Locate every blood parasite and identify its species.
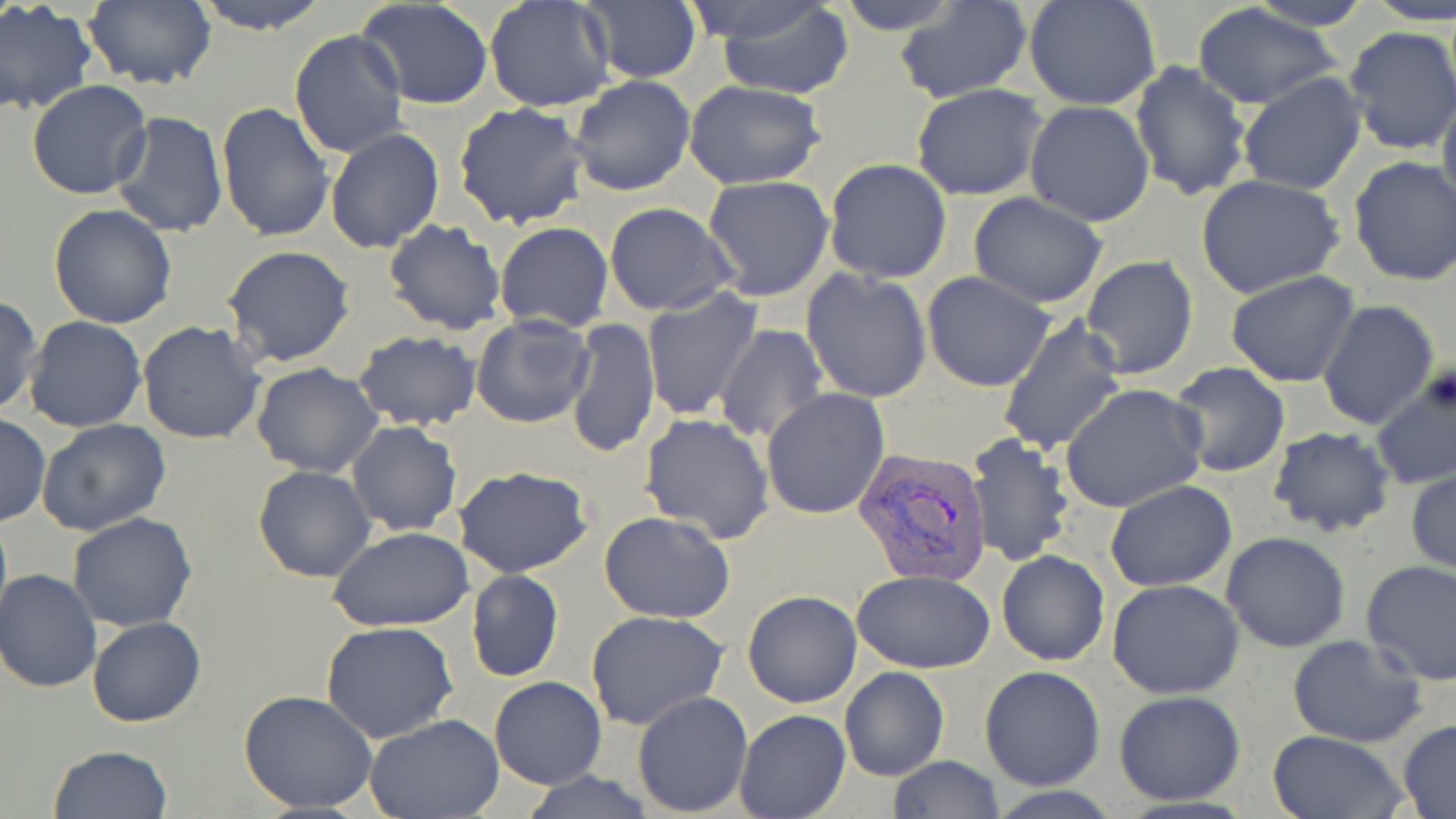

Approximate bounding boxes as [x1, y1, x2, y2] in pixels.
Plasmodium vivax-infected red blood cells: [852, 447, 991, 588].
No Plasmodium falciparum, Plasmodium ovale, Plasmodium malariae, Babesia divergens, or Trypanosoma brucei observed.

slide_level_diagnosis: Plasmodium vivax
preparation: thin blood film
modality: optical microscopy
image_size: 1456×819 pixels
stain: May-Grünwald-Giemsa
uninfected_red_blood_cell_locations: 'approximate bounding boxes as [x1, y1, x2, y2] in pixels: [80, 0, 217, 90], [183, 0, 334, 35], [714, 0, 855, 99], [838, 0, 960, 31], [1023, 0, 1164, 111], [1242, 0, 1373, 30], [1366, 0, 1454, 26], [485, 1, 618, 112], [895, 1, 1034, 104], [356, 2, 494, 109], [576, 2, 704, 84], [0, 3, 97, 116], [1191, 5, 1343, 109], [1341, 26, 1455, 157], [289, 29, 410, 160], [1128, 61, 1253, 201], [1238, 72, 1368, 193], [569, 74, 696, 196], [27, 80, 154, 200], [682, 80, 826, 188], [1437, 84, 1456, 218], [911, 85, 1047, 202], [216, 101, 336, 244], [453, 101, 590, 231], [1024, 101, 1156, 227], [111, 110, 230, 238], [324, 127, 444, 254], [1347, 156, 1456, 287], [823, 158, 952, 283], [1196, 174, 1346, 300], [702, 175, 834, 301], [968, 193, 1109, 309], [618, 197, 747, 418], [603, 203, 737, 316], [46, 204, 177, 330], [383, 219, 507, 335], [494, 221, 614, 332], [222, 246, 356, 368], [1079, 254, 1200, 379], [801, 268, 934, 403], [922, 270, 1056, 392], [1227, 271, 1360, 387], [641, 288, 762, 421], [0, 296, 43, 416], [1317, 300, 1439, 432], [471, 313, 595, 429], [23, 316, 147, 434], [997, 316, 1127, 457], [565, 318, 661, 459], [138, 319, 267, 445], [715, 324, 829, 446], [354, 330, 481, 433], [1169, 362, 1290, 478], [251, 363, 383, 478], [1371, 368, 1455, 490], [1060, 384, 1207, 514], [762, 388, 893, 520], [639, 413, 775, 542], [0, 414, 49, 526], [36, 420, 170, 537], [347, 421, 462, 535], [1267, 426, 1396, 538], [964, 433, 1077, 568], [252, 465, 375, 584], [455, 465, 593, 577], [1407, 470, 1455, 576], [1105, 481, 1238, 590], [0, 507, 12, 633], [68, 512, 198, 632], [599, 512, 735, 623], [328, 526, 476, 633], [1220, 532, 1350, 653], [995, 549, 1109, 666], [1361, 558, 1456, 683], [0, 569, 102, 693], [467, 569, 564, 683], [852, 570, 995, 674], [1107, 580, 1245, 699], [743, 590, 861, 709], [584, 609, 733, 732], [87, 616, 207, 727], [321, 621, 458, 744], [1286, 634, 1428, 748], [979, 665, 1106, 790], [839, 666, 950, 781], [489, 675, 606, 789], [239, 688, 379, 814], [1113, 689, 1245, 805], [632, 690, 753, 816], [734, 710, 851, 818], [365, 714, 505, 819], [1397, 720, 1456, 816], [1265, 731, 1410, 819], [48, 745, 173, 819], [886, 755, 1005, 819], [519, 769, 657, 819]'
field_of_view: single
magnification: 1000x